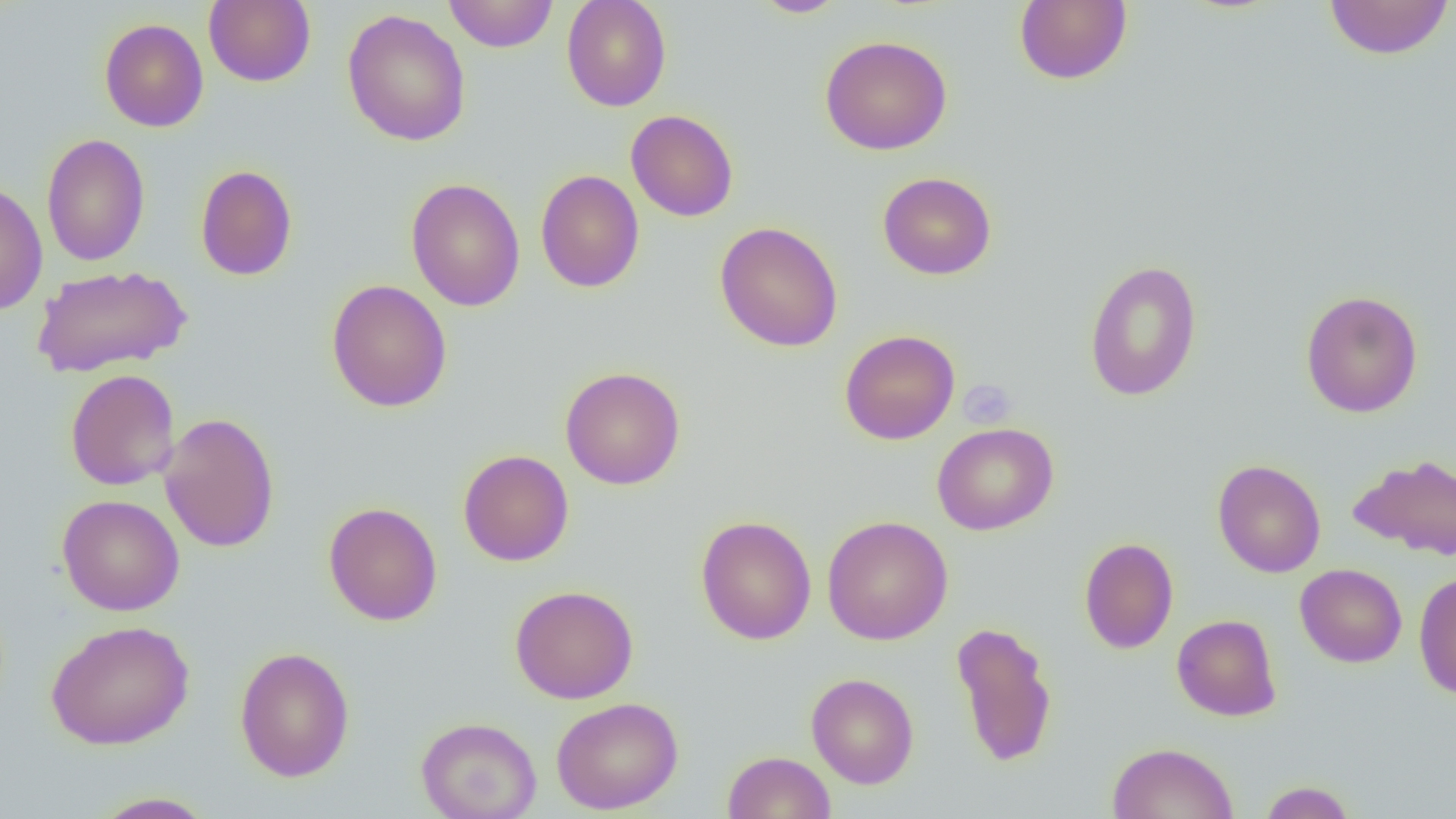
Summary:
  - Coordinate format: approximate bounding boxes as named x1/y1/x2/y2 corners in pixels
  - Uninfected red blood cell locations: (x1=203, y1=0, x2=316, y2=88), (x1=443, y1=0, x2=559, y2=53), (x1=561, y1=0, x2=672, y2=111), (x1=749, y1=0, x2=849, y2=18), (x1=1014, y1=0, x2=1132, y2=86), (x1=1323, y1=0, x2=1454, y2=60), (x1=342, y1=9, x2=471, y2=146), (x1=99, y1=17, x2=209, y2=132), (x1=819, y1=34, x2=953, y2=155), (x1=626, y1=109, x2=739, y2=222), (x1=41, y1=133, x2=150, y2=267), (x1=195, y1=164, x2=298, y2=281), (x1=535, y1=170, x2=645, y2=293), (x1=878, y1=171, x2=996, y2=280), (x1=406, y1=177, x2=525, y2=312), (x1=0, y1=179, x2=48, y2=316), (x1=714, y1=221, x2=843, y2=352), (x1=1083, y1=259, x2=1203, y2=401), (x1=31, y1=264, x2=193, y2=378), (x1=326, y1=279, x2=453, y2=412), (x1=1300, y1=289, x2=1423, y2=418), (x1=839, y1=329, x2=960, y2=445), (x1=559, y1=366, x2=686, y2=490), (x1=65, y1=369, x2=180, y2=490), (x1=159, y1=412, x2=280, y2=552), (x1=932, y1=422, x2=1059, y2=535), (x1=458, y1=449, x2=574, y2=566), (x1=1348, y1=453, x2=1456, y2=560), (x1=1212, y1=459, x2=1326, y2=578), (x1=57, y1=494, x2=184, y2=616), (x1=323, y1=501, x2=443, y2=626), (x1=695, y1=515, x2=817, y2=645), (x1=822, y1=515, x2=953, y2=645), (x1=1079, y1=537, x2=1179, y2=654), (x1=1295, y1=563, x2=1407, y2=667), (x1=1413, y1=570, x2=1456, y2=699), (x1=510, y1=584, x2=639, y2=704), (x1=1171, y1=614, x2=1282, y2=721), (x1=46, y1=619, x2=195, y2=750), (x1=950, y1=620, x2=1058, y2=767), (x1=234, y1=646, x2=355, y2=782), (x1=806, y1=672, x2=919, y2=788), (x1=552, y1=696, x2=683, y2=814), (x1=416, y1=716, x2=542, y2=819), (x1=1106, y1=741, x2=1238, y2=819), (x1=724, y1=751, x2=835, y2=819), (x1=1257, y1=780, x2=1357, y2=818), (x1=89, y1=791, x2=217, y2=818)
  - Platelet locations: (x1=958, y1=379, x2=1017, y2=429)
  - Slide-level diagnosis: no evidence of blood parasites
  - Preparation: thin blood film
  - Modality: light microscopy
  - Magnification: 1000x
  - Field of view: one of a larger specimen
  - Image size: 1456×819 pixels